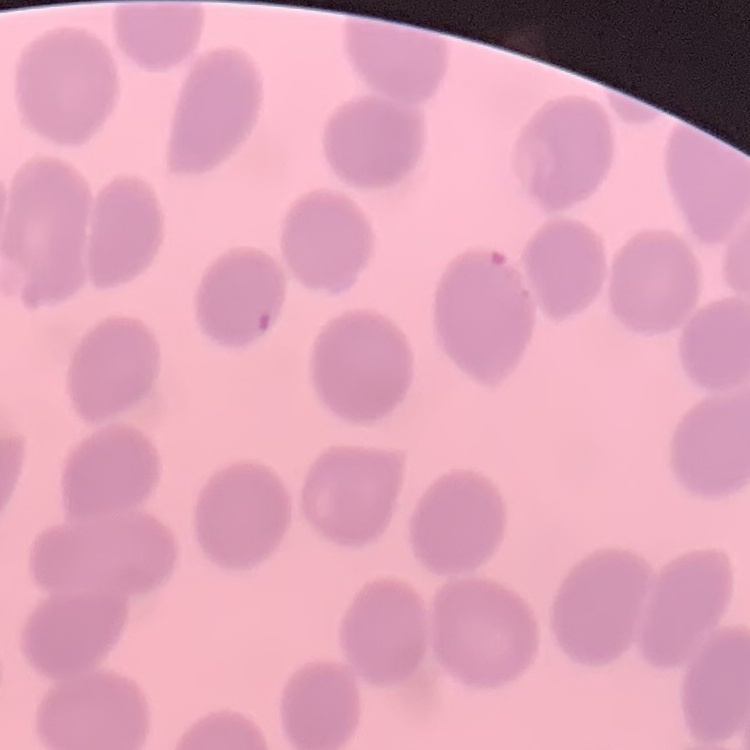

Summary:
  - Red blood cell morphology: no rouleaux formation
  - Stain: Field's or Giemsa
  - Image type: one tile cut from a larger photomicrograph
  - Preparation: thin blood smear